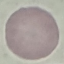

Summary:
  - Malaria status: uninfected
  - Image type: cell patch, automatically extracted from a larger field of view and resized to 64 × 64 pixels
  - Stain: Giemsa
  - Preparation: thin blood film
  - Capture: smartphone camera at the microscope eyepiece